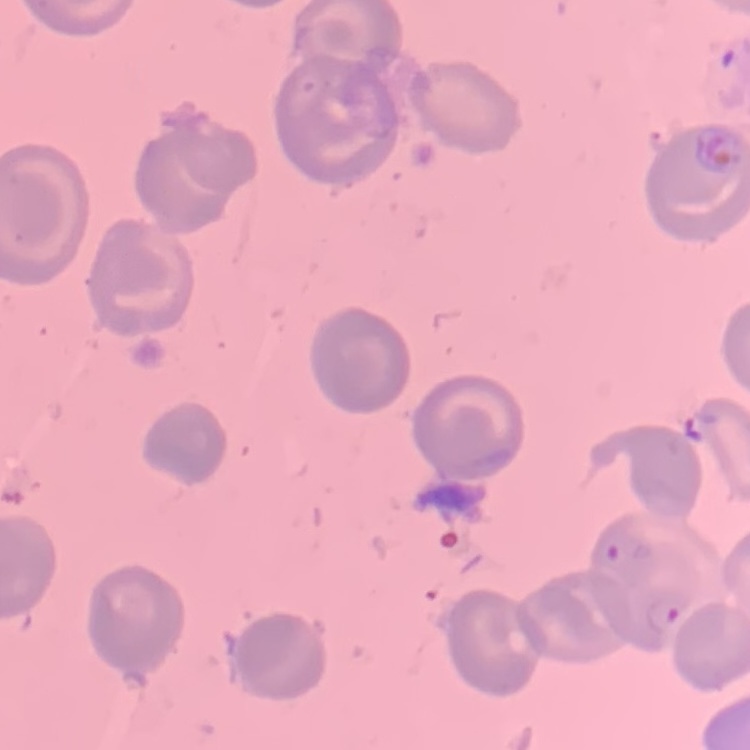
Summary:
  - Erythrocyte morphology: no rouleaux formation
  - Stain: Field's or Giemsa
  - Image type: one tile cut from a larger photomicrograph
  - Preparation: thin blood film